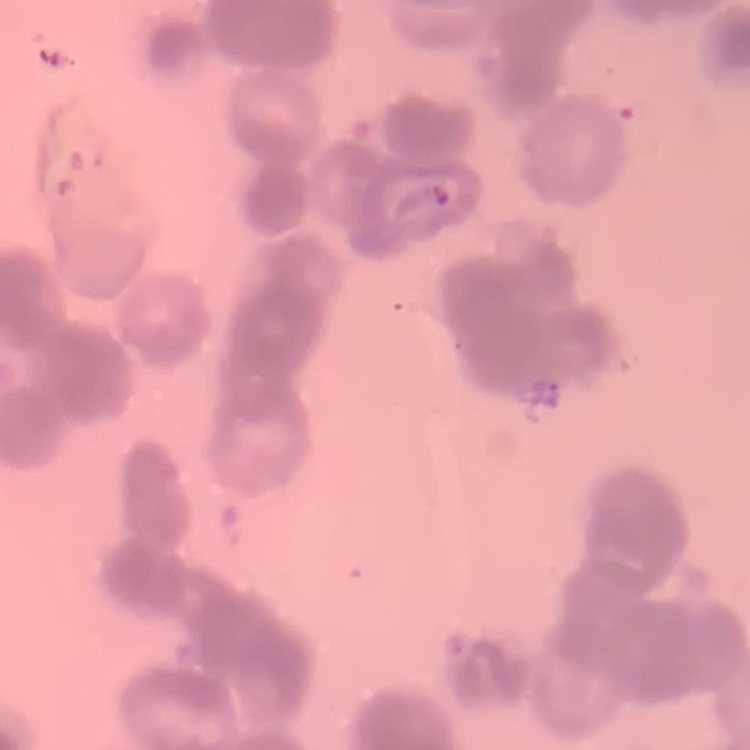 The red blood cells exhibit rouleaux formation. Stained with either Field's or Giemsa. Square crop of a larger photomicrograph. Thin blood smear.